Locate every Plasmodium ovale-infected red blood cell.
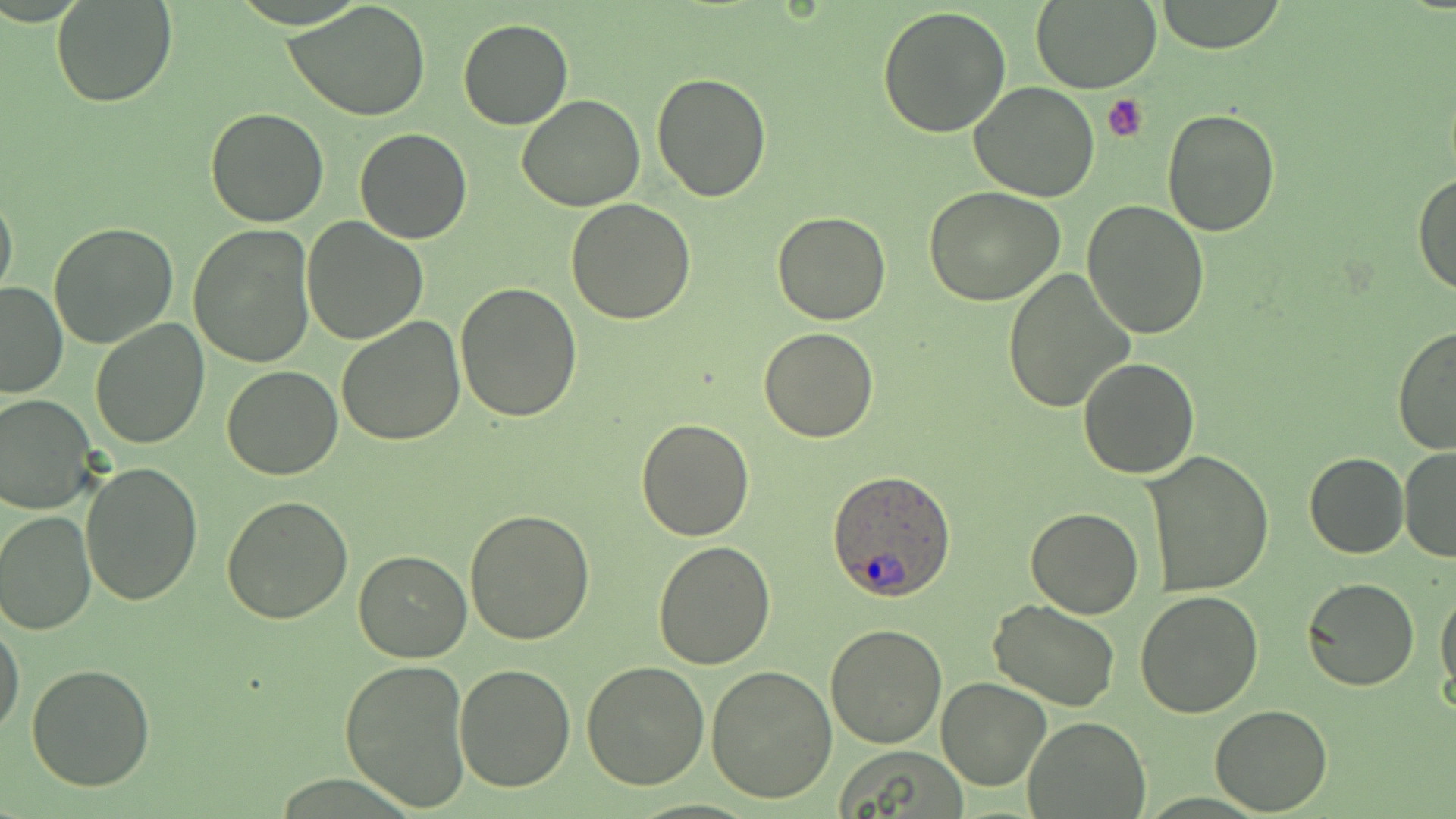
Approximate bounding boxes as (x1,y1)-(x2,y2) corner pairs in pixels.
Plasmodium ovale-infected red blood cells: (827,472)-(955,601).

Summary:
  - Uninfected red blood cell locations: (1032,0)-(1161,92), (51,1)-(178,108), (1153,1)-(1289,53), (284,2)-(431,121), (877,7)-(1011,139), (459,18)-(573,129), (650,72)-(773,203), (970,82)-(1099,202), (515,94)-(645,211), (205,106)-(329,227), (1161,109)-(1281,238), (355,127)-(472,244), (1414,173)-(1456,297), (0,184)-(18,305), (923,185)-(1065,305), (566,197)-(696,323), (1081,200)-(1211,339), (772,212)-(891,326), (301,217)-(428,344), (47,223)-(179,350), (186,223)-(314,368), (1001,270)-(1135,413), (456,281)-(583,421), (0,282)-(69,398), (335,316)-(465,447), (90,320)-(210,449), (1394,324)-(1456,457), (758,327)-(880,443), (1078,357)-(1199,479), (221,364)-(344,480), (0,393)-(98,514), (637,417)-(754,539), (1398,447)-(1456,562), (1142,451)-(1274,597), (1305,453)-(1407,558), (79,460)-(203,606), (222,496)-(354,625), (1025,506)-(1145,619), (465,508)-(597,645), (1,509)-(97,634), (653,540)-(778,668), (353,548)-(472,662), (1302,576)-(1419,691), (1435,586)-(1456,702), (1133,592)-(1263,718), (987,599)-(1120,711), (1,618)-(25,740), (825,624)-(947,748), (339,657)-(471,812), (581,660)-(710,791), (705,663)-(838,803), (27,664)-(157,790), (453,664)-(577,792), (935,675)-(1052,791), (1209,706)-(1334,814), (1022,717)-(1151,818), (832,746)-(971,817)
  - Platelet locations: (1102,94)-(1152,144)
  - Slide-level diagnosis: Plasmodium ovale
  - Preparation: thin blood smear
  - Magnification: 1000x
  - Field of view: one of a larger specimen
  - Image size: 1456×819 pixels
  - Stain: May-Grünwald-Giemsa
  - Modality: optical microscopy